State the blood parasite species.
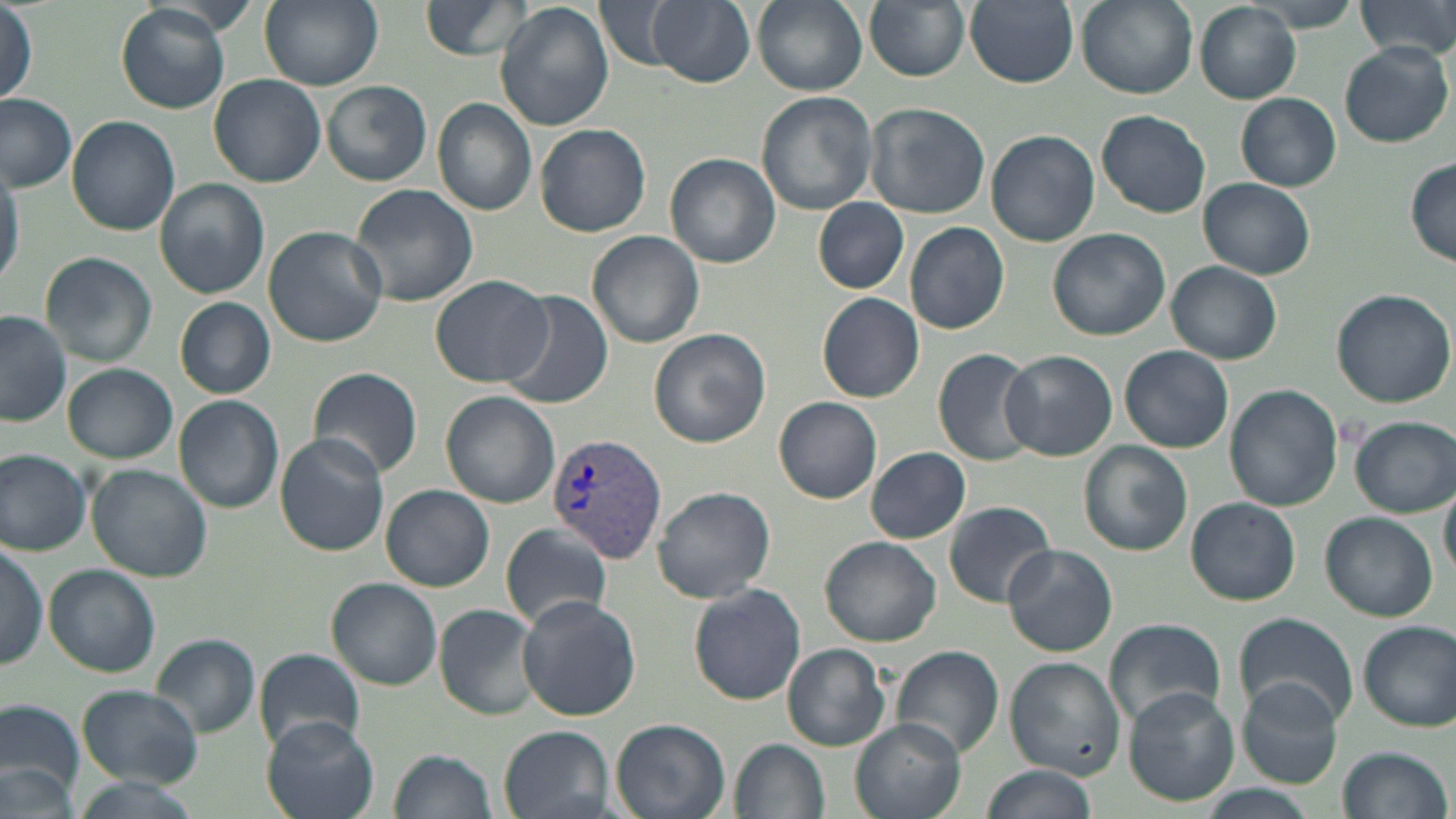
Plasmodium vivax.

{
  "uninfected_red_blood_cell_locations": "approximate bounding boxes as [x1, y1, x2, y2] in pixels: [258, 0, 383, 89], [421, 0, 539, 60], [595, 0, 686, 72], [648, 0, 754, 88], [752, 0, 866, 95], [864, 0, 971, 82], [966, 0, 1079, 88], [1076, 0, 1195, 98], [1244, 0, 1365, 34], [1356, 0, 1456, 62], [495, 3, 613, 133], [1194, 3, 1300, 105], [116, 4, 230, 113], [1, 8, 38, 109], [1338, 42, 1453, 147], [208, 73, 326, 187], [319, 79, 432, 185], [756, 92, 878, 214], [1236, 92, 1341, 191], [0, 94, 78, 193], [432, 98, 537, 218], [864, 101, 990, 219], [1097, 109, 1211, 218], [67, 116, 179, 235], [534, 122, 652, 236], [389, 125, 505, 268], [986, 129, 1100, 247], [667, 153, 779, 268], [0, 156, 22, 291], [1404, 159, 1456, 267], [155, 178, 269, 298], [1199, 178, 1315, 279], [347, 182, 478, 307], [813, 198, 908, 294], [904, 221, 1010, 334], [263, 227, 388, 348], [1048, 228, 1170, 341], [587, 231, 704, 348], [40, 253, 157, 368], [1168, 261, 1281, 364], [431, 275, 552, 387], [1329, 288, 1455, 407], [501, 290, 613, 409], [817, 292, 924, 402], [175, 297, 277, 398], [0, 310, 73, 426], [648, 328, 772, 448], [1119, 345, 1234, 453], [932, 348, 1043, 468], [1000, 350, 1118, 462], [63, 364, 176, 463], [308, 367, 423, 478], [1225, 385, 1342, 513], [441, 392, 560, 509], [173, 395, 283, 512], [774, 396, 882, 503], [1350, 416, 1454, 516], [274, 434, 391, 555], [1078, 441, 1193, 555], [866, 446, 972, 544], [0, 449, 92, 556], [86, 464, 213, 582], [1440, 476, 1456, 585], [382, 484, 494, 592], [653, 485, 776, 605], [1186, 497, 1300, 605], [944, 501, 1056, 608], [1321, 511, 1437, 620], [501, 522, 613, 633], [821, 536, 942, 647], [0, 544, 47, 669], [1002, 544, 1118, 656], [44, 564, 159, 676], [327, 577, 443, 689], [689, 584, 805, 704], [516, 595, 640, 720], [434, 604, 543, 720], [1233, 614, 1357, 729], [1103, 619, 1229, 730], [1357, 621, 1455, 731], [149, 634, 260, 738], [782, 643, 891, 751], [890, 644, 1004, 761], [255, 649, 366, 753], [1006, 657, 1126, 777], [1238, 678, 1344, 790], [77, 684, 203, 787], [1120, 685, 1238, 806], [0, 698, 86, 808], [260, 717, 379, 818], [610, 717, 731, 819], [851, 718, 964, 819], [499, 726, 614, 819], [731, 739, 829, 819], [1336, 746, 1450, 819], [390, 748, 496, 819], [0, 761, 78, 818], [979, 764, 1095, 819], [68, 778, 200, 819], [1193, 785, 1321, 818]",
  "plasmodium_vivax_infected_red_blood_cell_locations": "approximate bounding boxes as [x1, y1, x2, y2] in pixels: [548, 432, 667, 563]",
  "magnification": "1000x",
  "preparation": "thin blood film",
  "modality": "optical microscopy",
  "image_size": "1456×819 pixels",
  "stain": "May-Grünwald-Giemsa",
  "field_of_view": "one of a larger specimen"
}